Assess this cell for malaria.
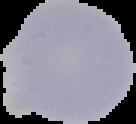

Uninfected.

image type = cell region segmented out of the field of view; surrounding area masked to black
preparation = thin blood film
image size = 136×124 pixels